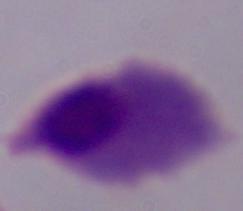

Summary:
  - Identification: trichomonad
  - Modality: micrograph
  - Magnification: 1000x